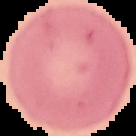

preparation = thin blood film
result = negative for Plasmodium parasites
image type = cell region segmented out of the field of view; surrounding area masked to black
image size = 136×136 pixels